Outline each blood parasite and name the species.
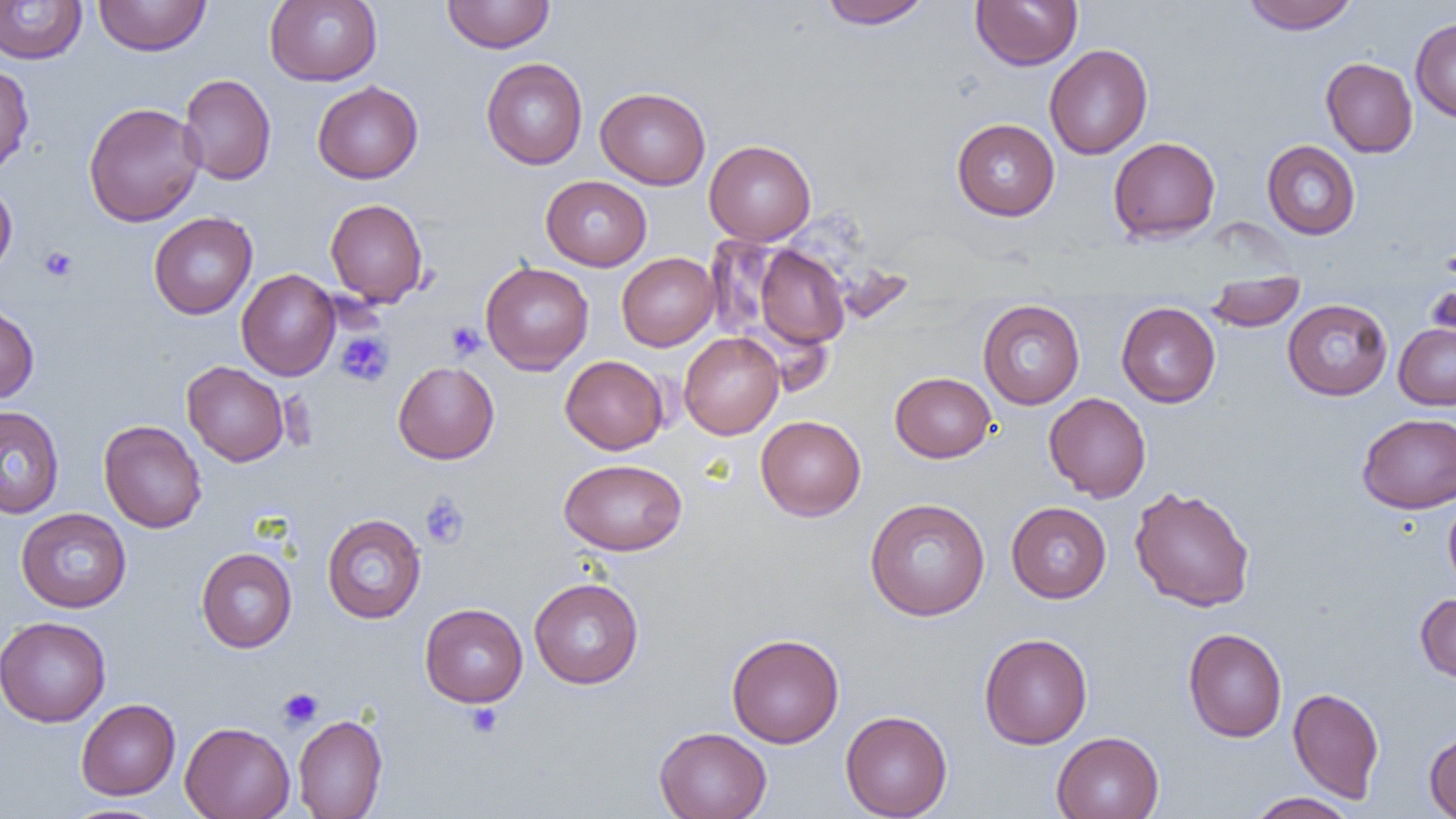

No blood parasites observed.

Summary:
  - Coordinate format: approximate bounding boxes as [x1, y1, x2, y2] in pixels
  - Uninfected red blood cell locations: [93, 0, 212, 56], [264, 0, 382, 86], [442, 0, 555, 53], [819, 0, 931, 29], [970, 0, 1082, 71], [1242, 0, 1358, 34], [0, 1, 87, 64], [1410, 18, 1456, 123], [1044, 44, 1153, 159], [1320, 57, 1418, 158], [481, 58, 587, 170], [0, 64, 34, 176], [178, 73, 277, 185], [312, 81, 423, 184], [595, 87, 711, 189], [83, 101, 205, 227], [951, 118, 1060, 221], [1108, 136, 1221, 242], [704, 139, 816, 245], [1261, 140, 1361, 240], [541, 176, 652, 271], [0, 179, 17, 278], [325, 198, 429, 307], [148, 212, 258, 319], [752, 244, 850, 348], [616, 252, 719, 351], [480, 261, 594, 375], [236, 268, 340, 380], [1204, 276, 1306, 331], [1426, 283, 1456, 347], [977, 299, 1085, 409], [1282, 299, 1393, 401], [1116, 301, 1220, 408], [0, 303, 39, 404], [1394, 323, 1456, 410], [679, 332, 784, 439], [560, 355, 669, 454], [182, 361, 289, 466], [393, 361, 499, 463], [890, 371, 996, 462], [1043, 392, 1151, 502], [0, 406, 65, 519], [1357, 413, 1456, 513], [755, 415, 866, 521], [98, 420, 207, 533], [559, 458, 687, 555], [1129, 486, 1255, 612], [1444, 495, 1456, 592], [865, 497, 990, 620], [1006, 501, 1111, 603], [16, 507, 131, 613], [321, 513, 427, 624], [196, 547, 297, 652], [529, 577, 644, 689], [1416, 593, 1456, 682], [420, 603, 528, 707], [0, 616, 111, 727], [1183, 628, 1287, 742], [978, 632, 1093, 749], [726, 633, 845, 748], [1288, 687, 1384, 803], [76, 698, 180, 800], [840, 710, 952, 818], [293, 713, 387, 819], [180, 721, 295, 819], [654, 726, 772, 819], [1424, 730, 1456, 819], [1051, 731, 1164, 819], [1246, 792, 1359, 819], [59, 804, 171, 819]
  - Platelet locations: [40, 246, 78, 282], [1441, 247, 1456, 282], [446, 321, 485, 360], [335, 331, 393, 386], [421, 493, 470, 547], [277, 688, 323, 729], [465, 703, 503, 738]
  - Slide-level diagnosis: negative for blood parasites
  - Field of view: one of a larger specimen
  - Preparation: thin blood smear
  - Image size: 1456×819 pixels
  - Magnification: 1000x
  - Modality: light microscopy